Describe the morphology of the red blood cells.
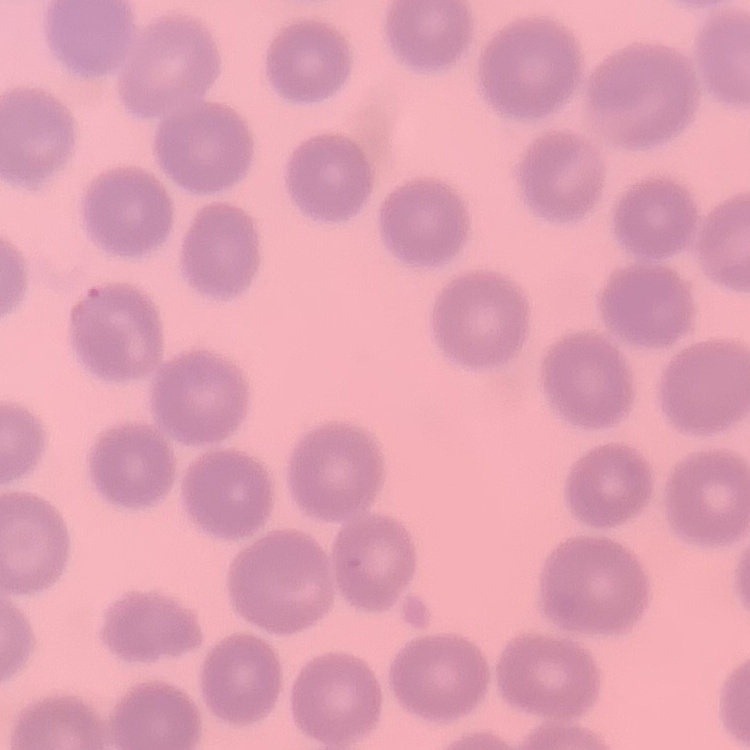
They show no rouleaux formation.

image type = one tile cut from a larger photomicrograph
stain = Field's or Giemsa
preparation = thin blood smear